State which parasite is depicted.
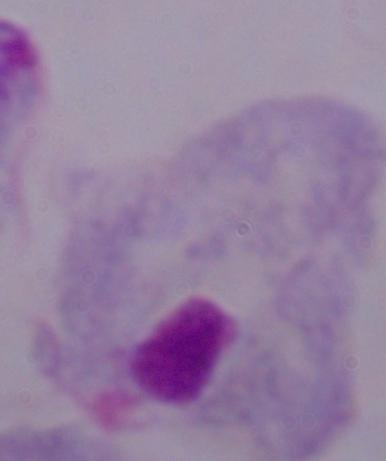
A trichomonad.

1000x magnification. Micrograph.